Identify the parasite.
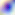

Toxoplasma gondii.

Summary:
  - Modality: micrograph
  - Magnification: 400x